Classify this cell by malaria status.
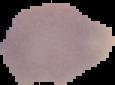

It is uninfected.

Summary:
  - Image type: cell region segmented out of the field of view; surrounding area masked to black
  - Image size: 115×85 pixels
  - Preparation: thin blood film